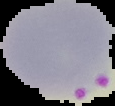

malaria status = parasitized
image size = 115×106 pixels
preparation = thin blood film
image type = cell region segmented out of the field of view; surrounding area masked to black